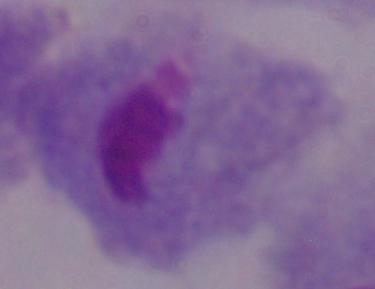

1000x magnification. A trichomonad is seen. Micrograph.